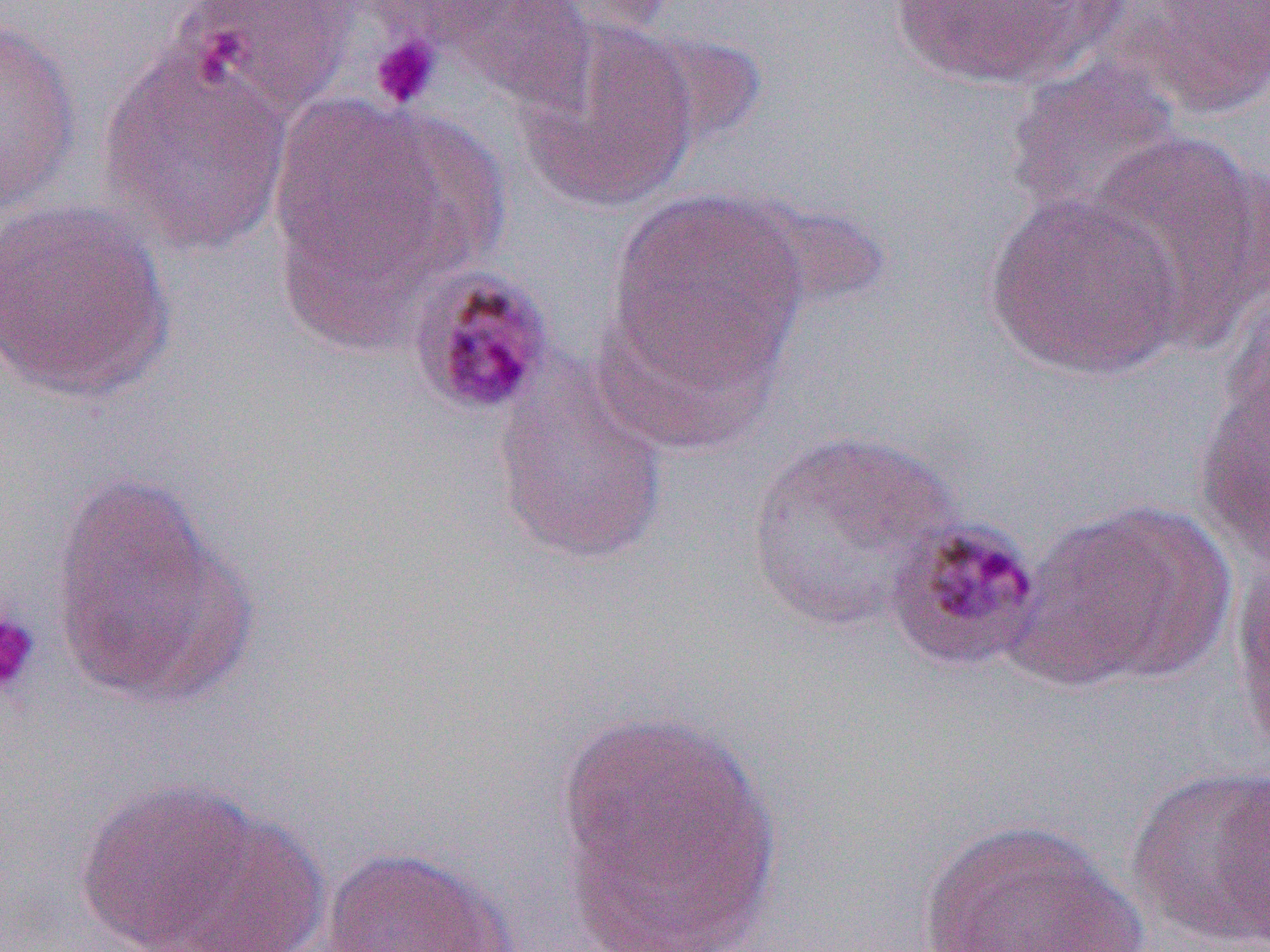 Approximate bounding boxes as named x1/y1/x2/y2 corners in pixels. Uninfected red blood cell locations: (x1=179, y1=0, x2=358, y2=115), (x1=438, y1=0, x2=598, y2=115), (x1=884, y1=0, x2=1126, y2=90), (x1=1131, y1=0, x2=1270, y2=118), (x1=0, y1=17, x2=82, y2=212), (x1=513, y1=19, x2=702, y2=212), (x1=99, y1=42, x2=296, y2=258), (x1=1004, y1=56, x2=1183, y2=221), (x1=264, y1=92, x2=492, y2=335), (x1=1080, y1=128, x2=1270, y2=348), (x1=603, y1=187, x2=812, y2=415), (x1=980, y1=191, x2=1189, y2=382), (x1=0, y1=197, x2=176, y2=403), (x1=1223, y1=277, x2=1270, y2=445), (x1=491, y1=355, x2=671, y2=567), (x1=1193, y1=372, x2=1269, y2=567), (x1=742, y1=430, x2=961, y2=635), (x1=48, y1=473, x2=254, y2=712), (x1=1014, y1=500, x2=1236, y2=689), (x1=1232, y1=544, x2=1270, y2=765), (x1=554, y1=707, x2=783, y2=952), (x1=1126, y1=764, x2=1270, y2=950), (x1=1215, y1=770, x2=1269, y2=952), (x1=75, y1=778, x2=275, y2=950), (x1=143, y1=809, x2=332, y2=952), (x1=916, y1=816, x2=1147, y2=952), (x1=318, y1=845, x2=518, y2=951). Platelet locations (subset): (x1=369, y1=32, x2=442, y2=111), (x1=0, y1=608, x2=41, y2=700). Slide-level diagnosis: Plasmodium malariae. Image is 1270×952 pixels. Captured at 1000x magnification. Single field of view. Optical microscopy. Thin blood smear.